Assess the morphology of the erythrocytes.
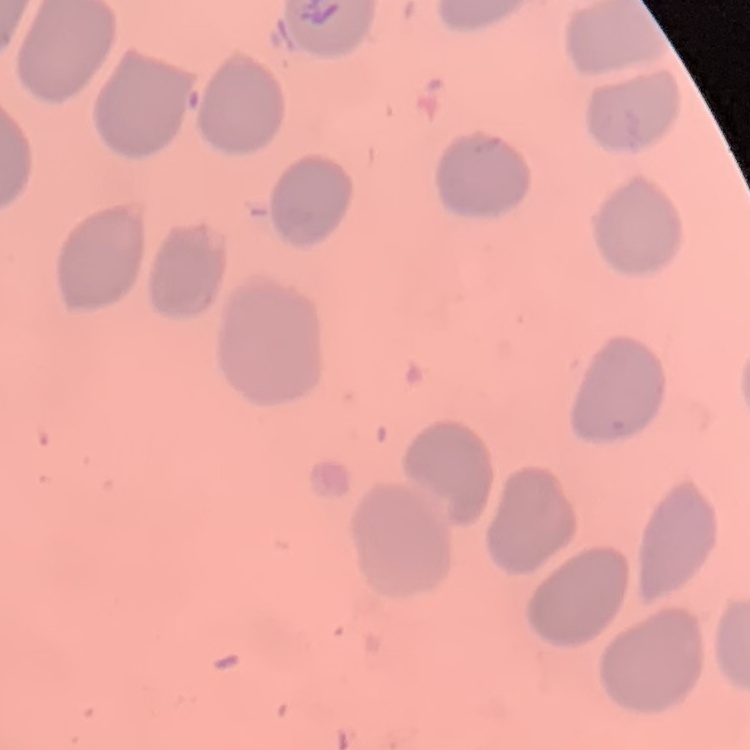

They show no rouleaux formation.

Square crop of a larger photomicrograph. Thin blood film. Field's or Giemsa stain.